Outline each blood parasite and name the species.
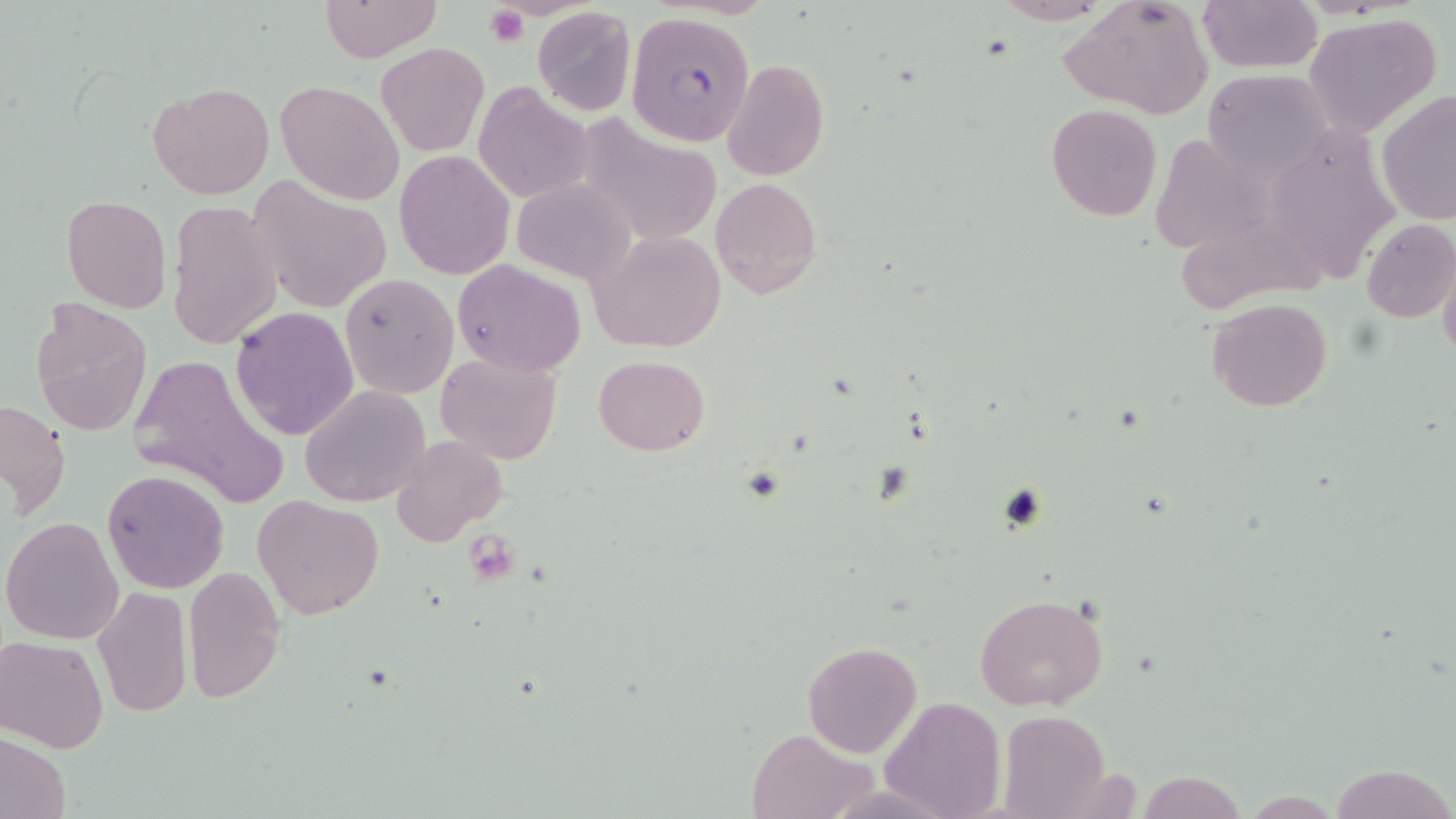
Approximate bounding boxes as [x1, y1, x2, y2] in pixels.
Plasmodium falciparum-infected red blood cells: [625, 16, 759, 145].
No Plasmodium ovale, Plasmodium malariae, Plasmodium vivax, Babesia divergens, or Trypanosoma brucei observed.

Summary:
  - Uninfected red blood cell locations: [320, 0, 439, 62], [987, 0, 1118, 25], [1197, 0, 1324, 72], [1063, 1, 1213, 120], [532, 6, 637, 115], [1302, 13, 1442, 137], [376, 42, 489, 158], [720, 59, 829, 183], [1202, 71, 1327, 179], [277, 79, 402, 205], [472, 81, 593, 203], [146, 82, 275, 199], [1377, 89, 1456, 226], [1046, 104, 1162, 221], [578, 120, 723, 247], [1278, 130, 1405, 281], [1151, 134, 1273, 257], [394, 150, 516, 280], [712, 177, 823, 299], [513, 178, 635, 283], [247, 181, 392, 314], [61, 194, 173, 313], [168, 203, 283, 351], [1360, 216, 1455, 323], [1180, 220, 1343, 319], [590, 232, 725, 351], [1439, 254, 1456, 369], [453, 259, 584, 375], [339, 275, 458, 399], [1205, 297, 1333, 412], [29, 300, 153, 438], [231, 305, 360, 440], [125, 353, 291, 515], [435, 353, 560, 464], [594, 355, 710, 455], [299, 384, 431, 508], [1, 399, 70, 518], [391, 435, 507, 548], [102, 469, 230, 594], [253, 495, 384, 620], [2, 517, 124, 644], [183, 567, 285, 702], [91, 585, 192, 719], [975, 594, 1108, 712], [1, 636, 111, 753], [802, 640, 922, 758], [879, 696, 1005, 819], [999, 710, 1108, 818], [747, 727, 874, 819], [0, 733, 72, 819], [1330, 763, 1452, 819], [1140, 772, 1244, 819]
  - Platelet locations: [486, 6, 528, 45], [467, 535, 520, 583]
  - Slide-level diagnosis: Plasmodium falciparum
  - Modality: optical microscopy
  - Image size: 1456×819 pixels
  - Magnification: 1000x
  - Field of view: one of a larger specimen
  - Preparation: thin blood film
  - Stain: May-Grünwald-Giemsa